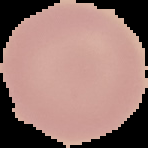
Summary:
  - Preparation: thin blood film
  - Image size: 148×148 pixels
  - Malaria status: uninfected
  - Image type: segmented cell region with the area outside set to black